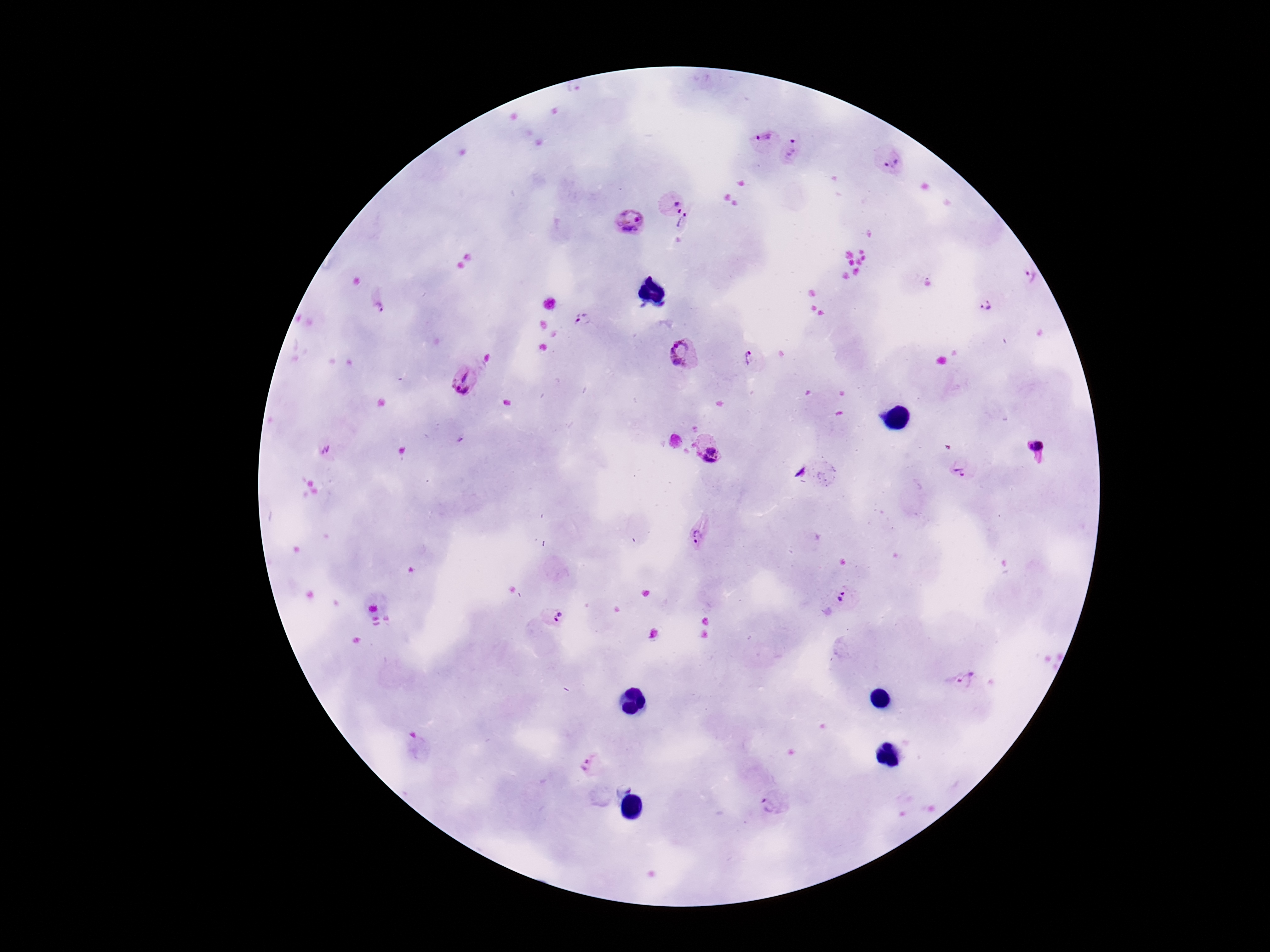

Approximate centers as (x, y) in pixels.
Summary:
  - Plasmodium parasite locations: (763, 137), (794, 151), (892, 161), (672, 200), (626, 220), (688, 224), (1031, 276), (985, 304), (378, 305), (583, 321), (683, 356), (749, 358), (465, 382), (1037, 449), (707, 450), (962, 468), (696, 537), (845, 598), (555, 616), (966, 678), (590, 765), (775, 802)
  - Preparation: thick peripheral-blood smear
  - Patient malaria status: positive
  - Magnification: 100x
  - Image size: 1270×952 pixels
  - Capture: smartphone camera through the microscope eyepiece
  - Stain: Giemsa
  - Field of view: one from this slide